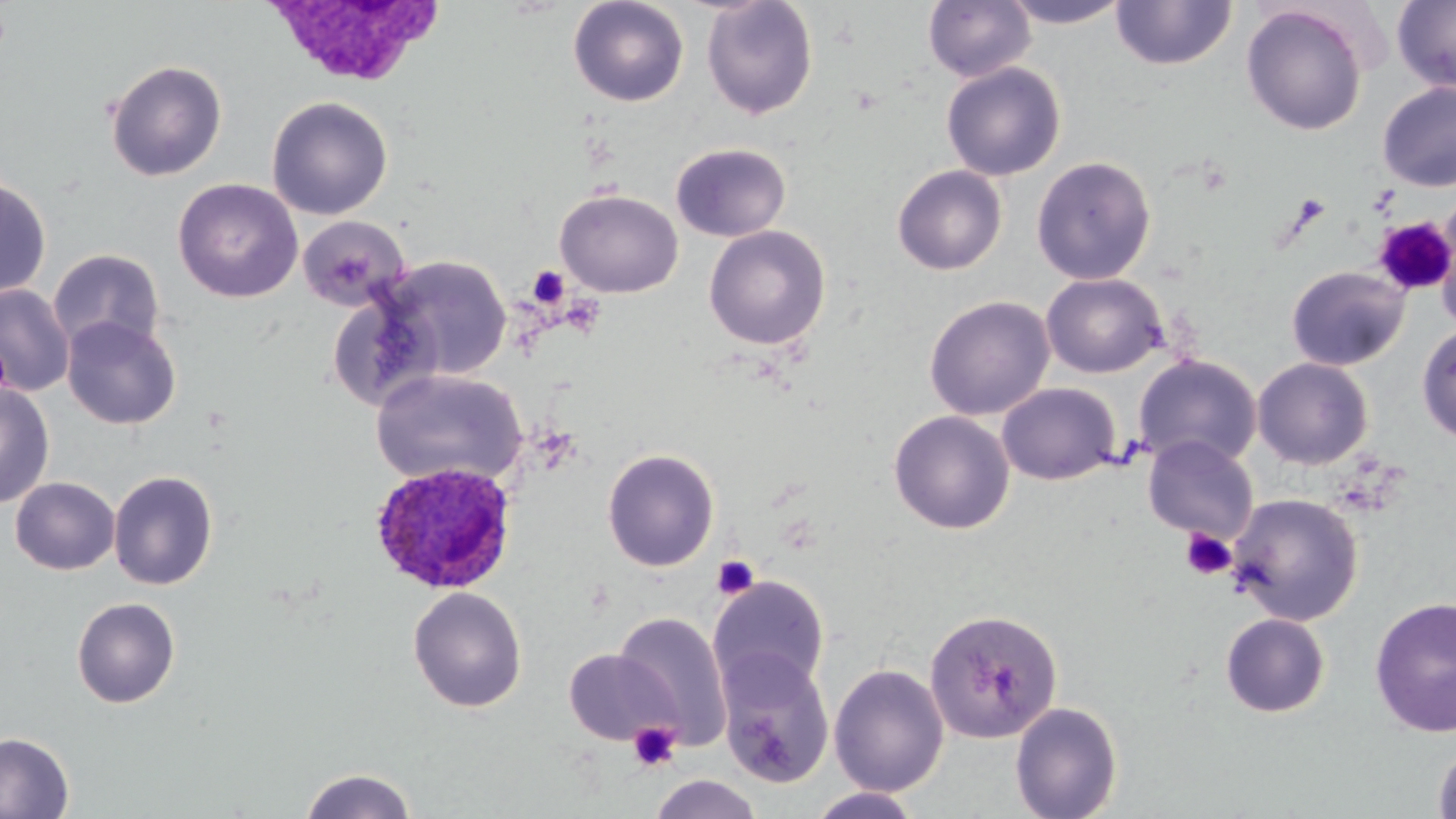

slide-level diagnosis = Plasmodium ovale
stain = May-Grünwald-Giemsa
uninfected red blood cell locations = approximate bounding boxes as [x1, y1, x2, y2] in pixels: [567, 0, 690, 107], [701, 0, 819, 119], [923, 0, 1036, 83], [1000, 0, 1133, 28], [1111, 0, 1237, 72], [1392, 0, 1456, 92], [1241, 4, 1368, 136], [105, 59, 227, 181], [941, 62, 1066, 181], [1377, 81, 1456, 192], [266, 96, 393, 220], [671, 142, 791, 242], [1031, 155, 1157, 285], [891, 164, 1008, 275], [1, 176, 52, 299], [172, 178, 303, 303], [555, 188, 683, 298], [1435, 210, 1456, 336], [298, 215, 410, 310], [703, 225, 831, 350], [48, 249, 166, 357], [377, 255, 511, 381], [1286, 265, 1411, 371], [1041, 272, 1167, 378], [0, 284, 74, 397], [924, 295, 1055, 421], [62, 316, 182, 430], [1417, 324, 1456, 443], [1133, 354, 1263, 471], [1252, 357, 1374, 469], [370, 369, 528, 489], [0, 381, 55, 509], [997, 382, 1121, 485], [888, 410, 1015, 535], [1142, 435, 1259, 543], [602, 448, 720, 572], [108, 470, 218, 590], [10, 476, 120, 575], [1226, 493, 1364, 626], [709, 576, 830, 697], [407, 586, 528, 712], [1368, 596, 1456, 738], [71, 597, 181, 708], [923, 607, 1063, 744], [611, 611, 732, 748], [1220, 613, 1331, 718], [564, 649, 679, 746], [716, 651, 835, 788], [829, 663, 949, 796], [1010, 701, 1123, 819], [0, 731, 75, 818], [1432, 742, 1456, 819], [298, 767, 419, 819], [648, 774, 763, 819], [806, 788, 925, 818]
field of view = single
modality = light microscopy
Plasmodium ovale-infected red blood cell locations = approximate bounding boxes as [x1, y1, x2, y2] in pixels: [370, 461, 518, 594]
platelet locations = approximate bounding boxes as [x1, y1, x2, y2] in pixels: [1372, 218, 1456, 295], [527, 266, 569, 309], [1180, 528, 1237, 581], [711, 555, 760, 600], [627, 721, 682, 772]
magnification = 1000x
image size = 1456×819 pixels
preparation = thin blood film